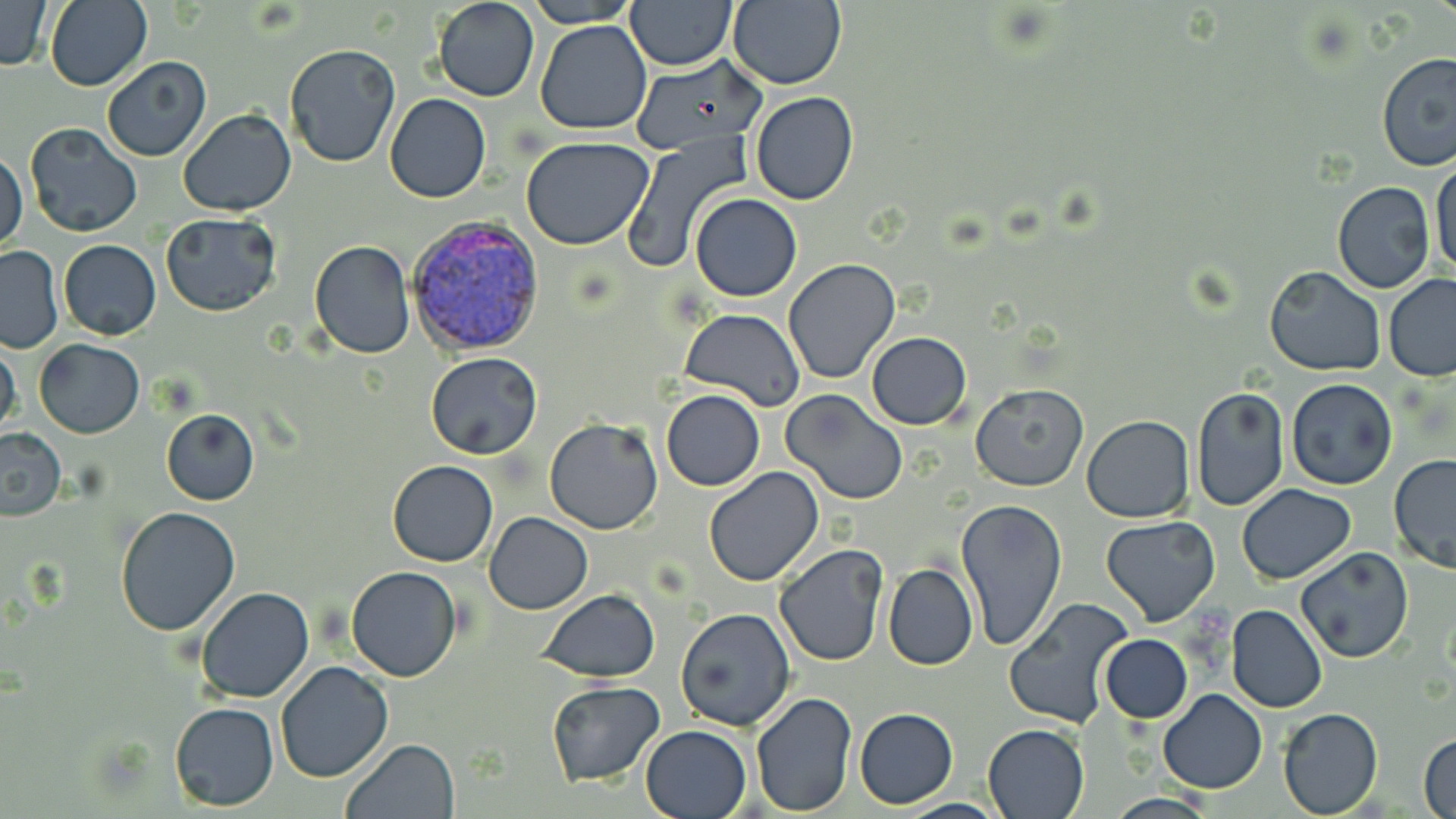

plasmodium_vivax_infected_red_blood_cell_locations: 'approximate bounding boxes as (x1, y1, x2, y2) in pixels: (408, 212, 546, 360)'
slide_level_diagnosis: Plasmodium vivax
field_of_view: one of a larger specimen
magnification: 1000x
stain: May-Grünwald-Giemsa
preparation: thin blood smear
modality: light microscopy
image_size: 1456×819 pixels
uninfected_red_blood_cell_locations: 'approximate bounding boxes as (x1, y1, x2, y2) in pixels: (433, 0, 539, 102), (522, 0, 639, 26), (624, 0, 738, 70), (0, 1, 52, 72), (44, 1, 152, 91), (726, 1, 848, 89), (533, 19, 653, 134), (284, 43, 400, 169), (1376, 51, 1456, 172), (633, 55, 767, 154), (102, 57, 212, 161), (384, 92, 491, 202), (750, 92, 859, 206), (178, 109, 297, 216), (23, 122, 142, 238), (521, 135, 655, 250), (621, 138, 747, 276), (0, 150, 29, 254), (1430, 155, 1456, 284), (1332, 181, 1436, 294), (690, 193, 801, 302), (160, 212, 282, 317), (58, 240, 161, 339), (309, 240, 416, 358), (0, 246, 62, 353), (783, 259, 900, 385), (1264, 266, 1385, 377), (1383, 275, 1456, 381), (681, 308, 804, 413), (865, 332, 972, 429), (0, 338, 22, 445), (34, 339, 145, 438), (425, 352, 542, 458), (1285, 379, 1398, 490), (970, 383, 1088, 491), (1192, 386, 1290, 511), (661, 389, 765, 492), (781, 390, 908, 504), (162, 409, 259, 505), (1091, 414, 1207, 624), (1082, 415, 1195, 522), (544, 419, 666, 535), (0, 428, 66, 519), (1388, 455, 1456, 575), (387, 460, 499, 567), (702, 467, 824, 587), (1237, 485, 1356, 582), (954, 497, 1068, 653), (114, 505, 241, 635), (485, 512, 593, 613), (1099, 516, 1220, 626), (774, 543, 889, 667), (1297, 547, 1414, 663), (883, 563, 978, 670), (346, 566, 463, 682), (195, 586, 314, 704), (538, 590, 659, 681), (1003, 598, 1136, 729), (1227, 605, 1328, 713), (676, 608, 796, 731), (1101, 635, 1192, 722), (275, 662, 392, 783), (545, 681, 665, 784), (1157, 689, 1268, 795), (749, 690, 858, 816), (170, 702, 278, 810), (855, 708, 958, 808), (1278, 708, 1384, 818), (641, 724, 752, 818), (983, 724, 1089, 818), (1418, 733, 1456, 819), (341, 738, 458, 819), (899, 798, 1005, 818)'